Describe the morphology of the erythrocytes.
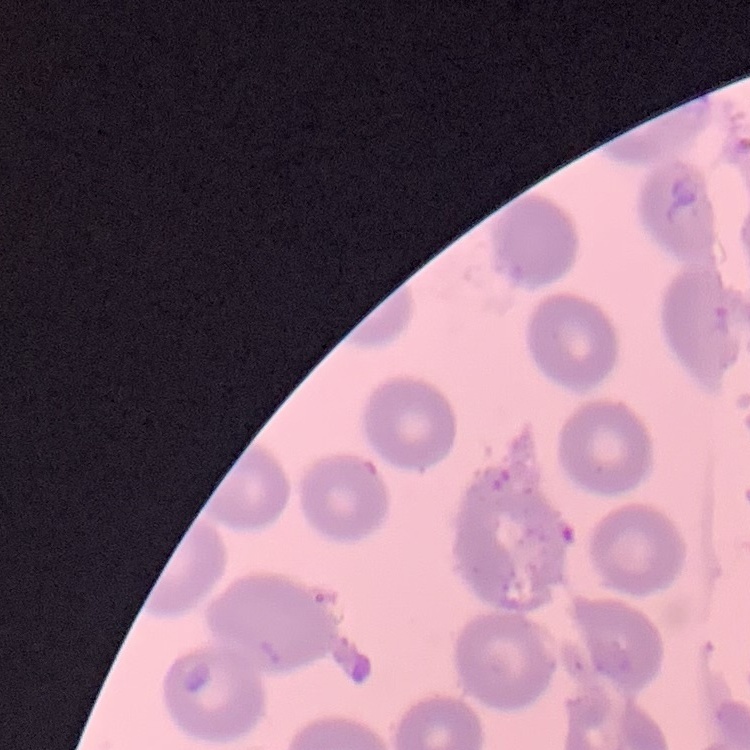
They show no rouleaux formation.

Thin peripheral smear. One tile cut from a larger photomicrograph. Field's or Giemsa stain.